Classify this cell by malaria status.
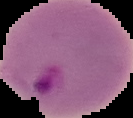

Parasitized.

Summary:
  - Preparation: thin blood film
  - Image size: 133×118 pixels
  - Image type: segmented cell region with the area outside set to black